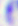

Summary:
  - Modality: micrograph
  - Identification: Toxoplasma gondii
  - Magnification: 400x